Locate every Trypanosoma brucei.
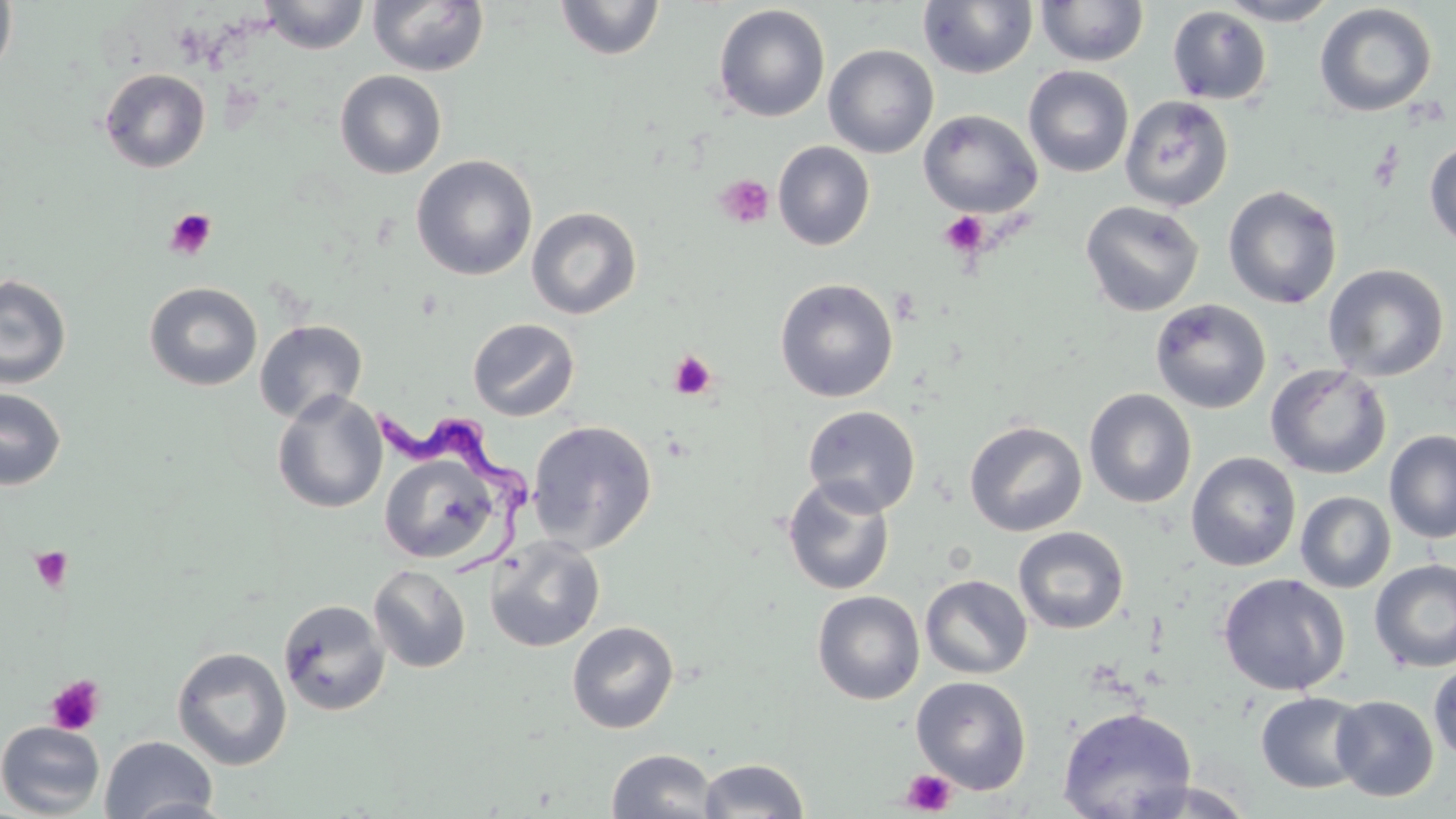
Approximate bounding boxes as [x1, y1, x2, y2] in pixels.
Trypanosoma brucei: [374, 399, 539, 581].

{
  "slide_level_diagnosis": "Trypanosoma brucei",
  "modality": "optical microscopy",
  "field_of_view": "single",
  "preparation": "thin blood film",
  "stain": "May-Grünwald-Giemsa",
  "image_size": "1456×819 pixels",
  "magnification": "1000x",
  "platelet_locations": "approximate bounding boxes as [x1, y1, x2, y2] in pixels: [715, 174, 775, 228], [165, 207, 217, 259], [939, 211, 990, 258], [668, 350, 717, 400], [30, 547, 73, 592], [45, 674, 105, 735], [900, 768, 956, 816]",
  "uninfected_red_blood_cell_locations": "approximate bounding boxes as [x1, y1, x2, y2] in pixels: [0, 0, 17, 85], [258, 0, 371, 54], [367, 0, 490, 78], [555, 0, 665, 61], [917, 0, 1038, 79], [1215, 0, 1341, 26], [1036, 1, 1149, 67], [1314, 3, 1437, 117], [712, 4, 831, 123], [1167, 5, 1273, 105], [824, 44, 939, 158], [1023, 65, 1134, 178], [99, 68, 211, 173], [335, 70, 447, 179], [1120, 95, 1234, 211], [918, 109, 1042, 218], [1424, 138, 1456, 250], [773, 141, 875, 251], [411, 154, 538, 281], [1223, 185, 1342, 309], [1080, 200, 1204, 316], [526, 206, 642, 319], [1323, 263, 1449, 381], [0, 274, 72, 389], [775, 278, 898, 402], [144, 281, 262, 391], [1150, 298, 1272, 414], [468, 317, 580, 421], [254, 320, 367, 424], [1265, 363, 1391, 479], [0, 387, 67, 490], [1083, 388, 1197, 508], [271, 390, 388, 514], [802, 405, 921, 516], [527, 420, 658, 553], [963, 420, 1087, 537], [1384, 431, 1456, 543], [1186, 451, 1301, 571], [378, 452, 502, 564], [782, 477, 896, 596], [1295, 491, 1396, 593], [1013, 526, 1129, 634], [485, 536, 606, 653], [1370, 559, 1456, 672], [368, 564, 472, 673], [1218, 573, 1350, 696], [920, 574, 1033, 679], [812, 590, 925, 705], [278, 598, 391, 717], [566, 621, 680, 734], [172, 646, 292, 771], [1428, 660, 1456, 763], [911, 676, 1032, 794], [1255, 691, 1371, 793], [1331, 695, 1439, 802], [1058, 707, 1198, 819], [0, 721, 105, 817], [99, 735, 218, 819], [606, 748, 719, 819], [697, 758, 809, 817], [1116, 777, 1260, 818], [124, 795, 239, 819]"
}